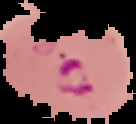

Summary:
  - Image size: 136×124 pixels
  - Preparation: thin blood smear
  - Malaria status: parasitized
  - Image type: segmented cell region with the area outside set to black